Identify the preparation type.
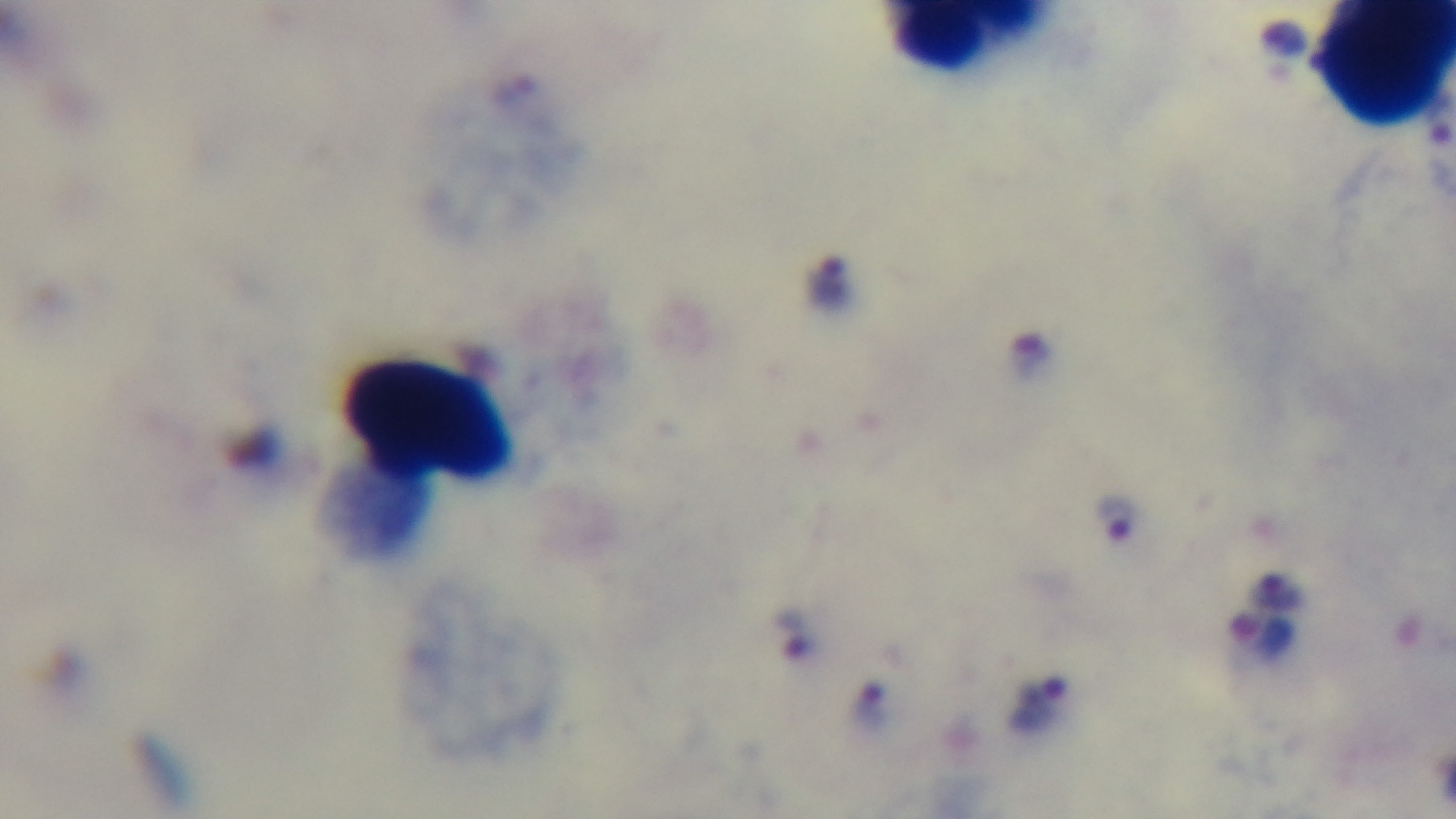
Thick.

field of view = single
stain = Giemsa
objective = 100x oil immersion
malaria status = infected
modality = light microscopy
capture = mounted 4K digital camera